Describe the morphology of the red blood cells.
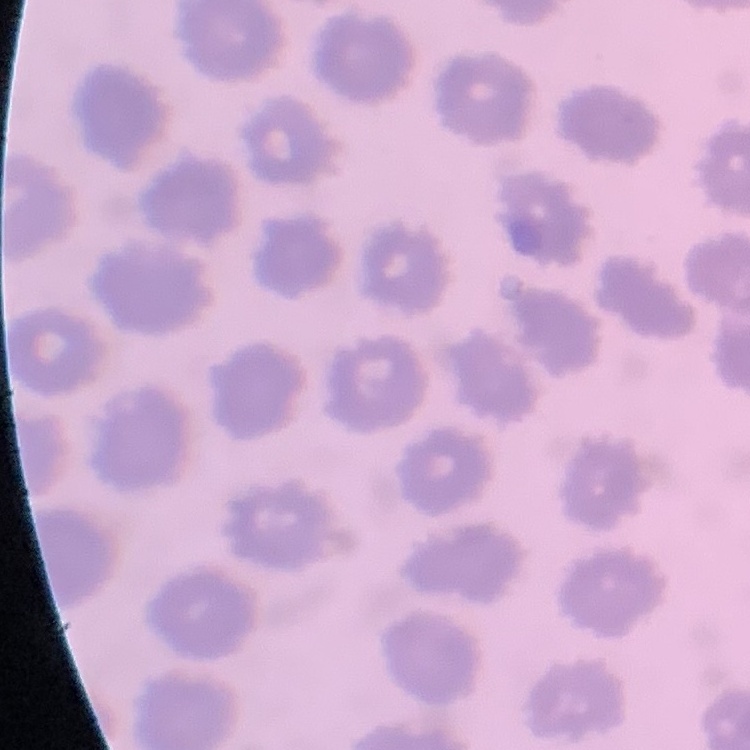
They show no rouleaux formation.

Summary:
  - Stain: Field's or Giemsa
  - Preparation: thin peripheral smear
  - Image type: square crop of a larger photomicrograph